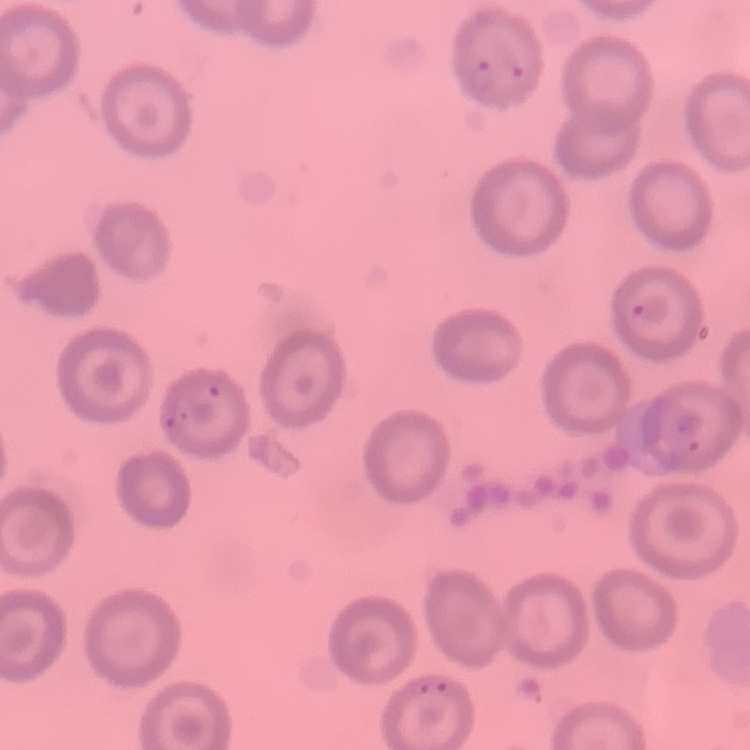
The red blood cells exhibit no rouleaux formation. Stained with either Field's or Giemsa. Thin blood film. One tile cut from a larger photomicrograph.